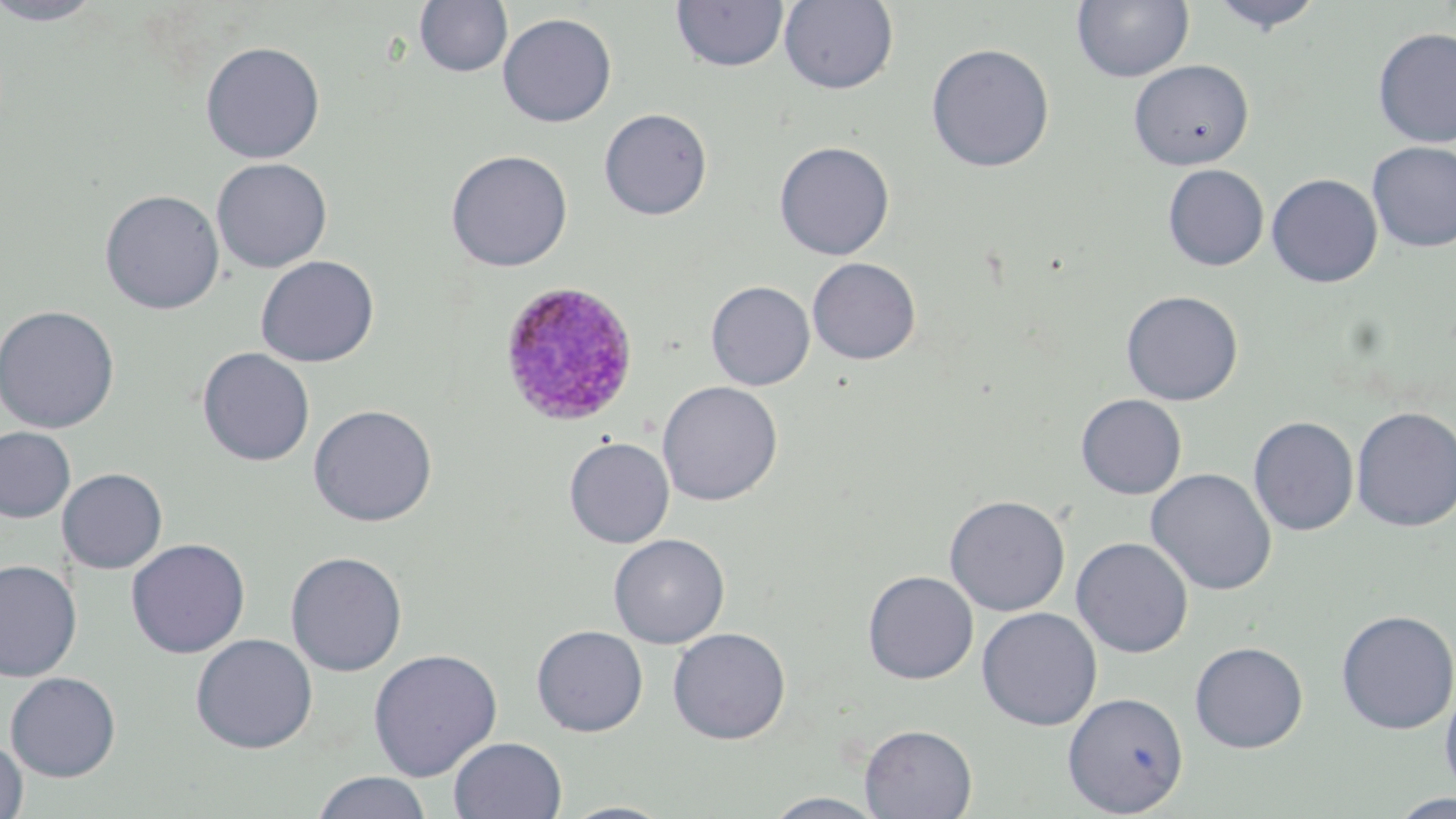

Approximate bounding boxes as (x1, y1, x2, y2) in pixels. Uninfected red blood cell locations: (0, 0, 108, 26), (414, 0, 513, 77), (779, 0, 899, 94), (1207, 0, 1327, 35), (671, 1, 789, 73), (1072, 1, 1195, 83), (497, 13, 618, 128), (1372, 27, 1456, 148), (199, 41, 326, 163), (925, 43, 1055, 173), (1128, 59, 1254, 170), (598, 108, 713, 220), (773, 141, 895, 261), (1366, 141, 1456, 252), (445, 149, 573, 272), (211, 157, 332, 273), (1162, 164, 1269, 271), (1266, 173, 1383, 288), (99, 189, 225, 315), (255, 255, 379, 368), (807, 258, 921, 365), (706, 280, 815, 390), (1121, 290, 1243, 406), (0, 305, 120, 433), (197, 347, 315, 467), (657, 381, 783, 506), (1075, 394, 1187, 500), (308, 404, 438, 527), (1351, 406, 1456, 532), (1248, 416, 1359, 535), (1, 426, 76, 523), (564, 437, 675, 548), (57, 468, 168, 574), (1146, 468, 1277, 596), (944, 495, 1071, 616), (609, 533, 730, 649), (1071, 537, 1194, 658), (126, 538, 250, 658), (285, 550, 408, 677), (0, 559, 82, 682), (862, 570, 978, 684), (976, 607, 1102, 731), (1335, 609, 1456, 735), (531, 625, 648, 737), (668, 627, 791, 744), (190, 633, 318, 753), (1189, 641, 1308, 753), (367, 648, 503, 781), (5, 671, 121, 781), (1440, 681, 1456, 799), (1063, 691, 1189, 817), (859, 724, 977, 819), (448, 736, 567, 819), (0, 737, 28, 819), (311, 771, 433, 819), (761, 792, 890, 818), (1387, 794, 1456, 819), (558, 801, 675, 819). Plasmodium ovale-infected red blood cell locations: (500, 282, 640, 429). Slide-level diagnosis: Plasmodium ovale. Image is 1456×819 pixels. Thin blood smear. Captured at 1000x magnification. Light microscopy. May-Grünwald-Giemsa-stained preparation. One field of a larger specimen.